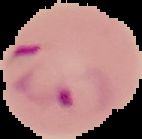
Cell region segmented out of the field of view; the surrounding area is masked to black. From a thin blood film. Malaria status: parasitized. Image is 142×139 pixels.